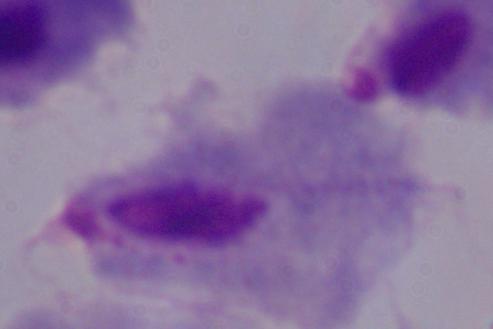

Summary:
  - Identification: trichomonad
  - Magnification: 1000x
  - Modality: photomicrograph